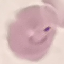

Summary:
  - Malaria status: parasitized
  - Stain: Giemsa
  - Capture: smartphone through the microscope eyepiece
  - Preparation: thin smear
  - Image type: automatically extracted cell patch, resized to 64 × 64 pixels